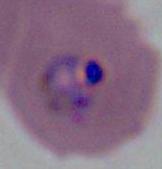
A Plasmodium parasite is shown. Photomicrograph. Captured at either 400x or 1000x magnification.